Assess this cell for malaria.
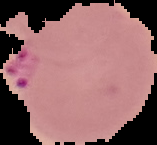
It is parasitized.

From a thin blood film. Image is 157×145 pixels. Segmented cell region on a black background.